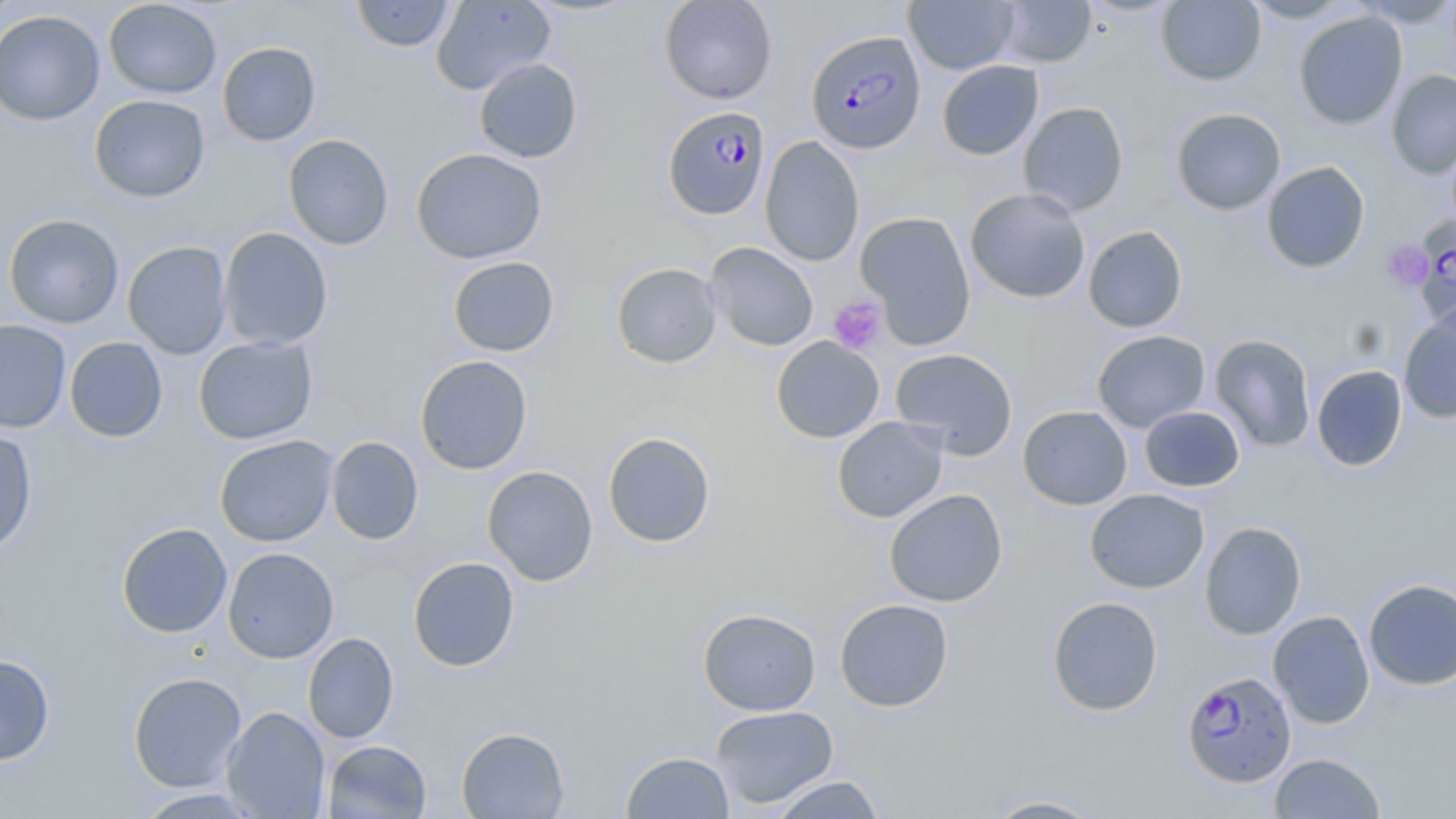
{
  "slide_level_diagnosis": "Plasmodium falciparum",
  "field_of_view": "single",
  "stain": "May-Grünwald-Giemsa",
  "modality": "optical microscopy",
  "magnification": "1000x",
  "uninfected_red_blood_cell_locations": "approximate bounding boxes as [x1, y1, x2, y2] in pixels: [0, 0, 23, 26], [103, 0, 222, 99], [351, 0, 457, 53], [431, 0, 555, 95], [659, 0, 777, 104], [903, 0, 1018, 75], [1156, 0, 1266, 86], [1242, 0, 1353, 23], [1352, 0, 1456, 27], [994, 1, 1097, 68], [0, 9, 106, 125], [1293, 11, 1408, 130], [217, 42, 321, 146], [474, 58, 583, 163], [937, 60, 1044, 160], [1386, 69, 1456, 180], [89, 94, 210, 202], [1018, 102, 1129, 216], [1171, 108, 1286, 215], [283, 134, 394, 250], [760, 136, 864, 267], [411, 147, 547, 264], [1261, 161, 1371, 273], [965, 188, 1090, 303], [855, 211, 976, 349], [3, 213, 124, 329], [1083, 225, 1187, 333], [219, 227, 333, 351], [122, 241, 233, 359], [705, 242, 819, 351], [448, 256, 559, 357], [611, 262, 722, 368], [1398, 309, 1456, 424], [0, 320, 72, 433], [1091, 330, 1211, 432], [1209, 333, 1317, 452], [194, 336, 318, 444], [771, 336, 884, 443], [65, 337, 168, 442], [890, 347, 1018, 459], [414, 355, 532, 475], [1311, 365, 1407, 471], [1018, 405, 1132, 510], [1139, 405, 1245, 492], [832, 417, 948, 523], [0, 429, 38, 556], [602, 431, 716, 548], [214, 435, 338, 547], [326, 436, 424, 545], [482, 465, 598, 586], [1085, 488, 1209, 593], [884, 489, 1008, 607], [1199, 521, 1307, 639], [116, 522, 233, 638], [223, 547, 339, 664], [407, 556, 520, 672], [1363, 578, 1456, 690], [1047, 596, 1163, 716], [834, 598, 954, 712], [698, 608, 821, 716], [1268, 611, 1375, 729], [303, 632, 399, 744], [0, 655, 55, 765], [128, 671, 247, 792], [709, 705, 839, 808], [221, 706, 330, 818], [456, 726, 570, 818], [323, 739, 432, 818], [621, 751, 735, 818], [1268, 752, 1387, 818], [769, 775, 887, 818], [132, 788, 266, 818], [979, 794, 1108, 818]",
  "plasmodium_falciparum_infected_red_blood_cell_locations": "approximate bounding boxes as [x1, y1, x2, y2] in pixels: [802, 32, 920, 157], [662, 105, 771, 220], [1404, 220, 1456, 320], [1181, 671, 1297, 787]",
  "platelet_locations": "approximate bounding boxes as [x1, y1, x2, y2] in pixels: [1382, 240, 1432, 292], [827, 295, 887, 355]",
  "image_size": "1456×819 pixels",
  "preparation": "thin blood film"
}